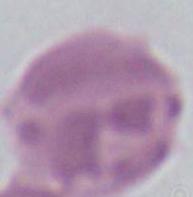

Summary:
  - Magnification: 1000x
  - Identification: erythrocyte
  - Modality: photomicrograph